Classify this cell by malaria status.
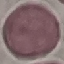

It is uninfected.

Cell patch, automatically extracted from a larger field of view and resized to 64 × 64 pixels. Photographed with a smartphone camera at the microscope eyepiece. Thin blood smear. Giemsa-stained preparation.